Assess this cell for malaria.
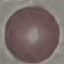

It is uninfected.

capture = smartphone through the microscope eyepiece
stain = Giemsa
preparation = thin blood smear
image type = automatically extracted cell patch, resized to 64 × 64 pixels